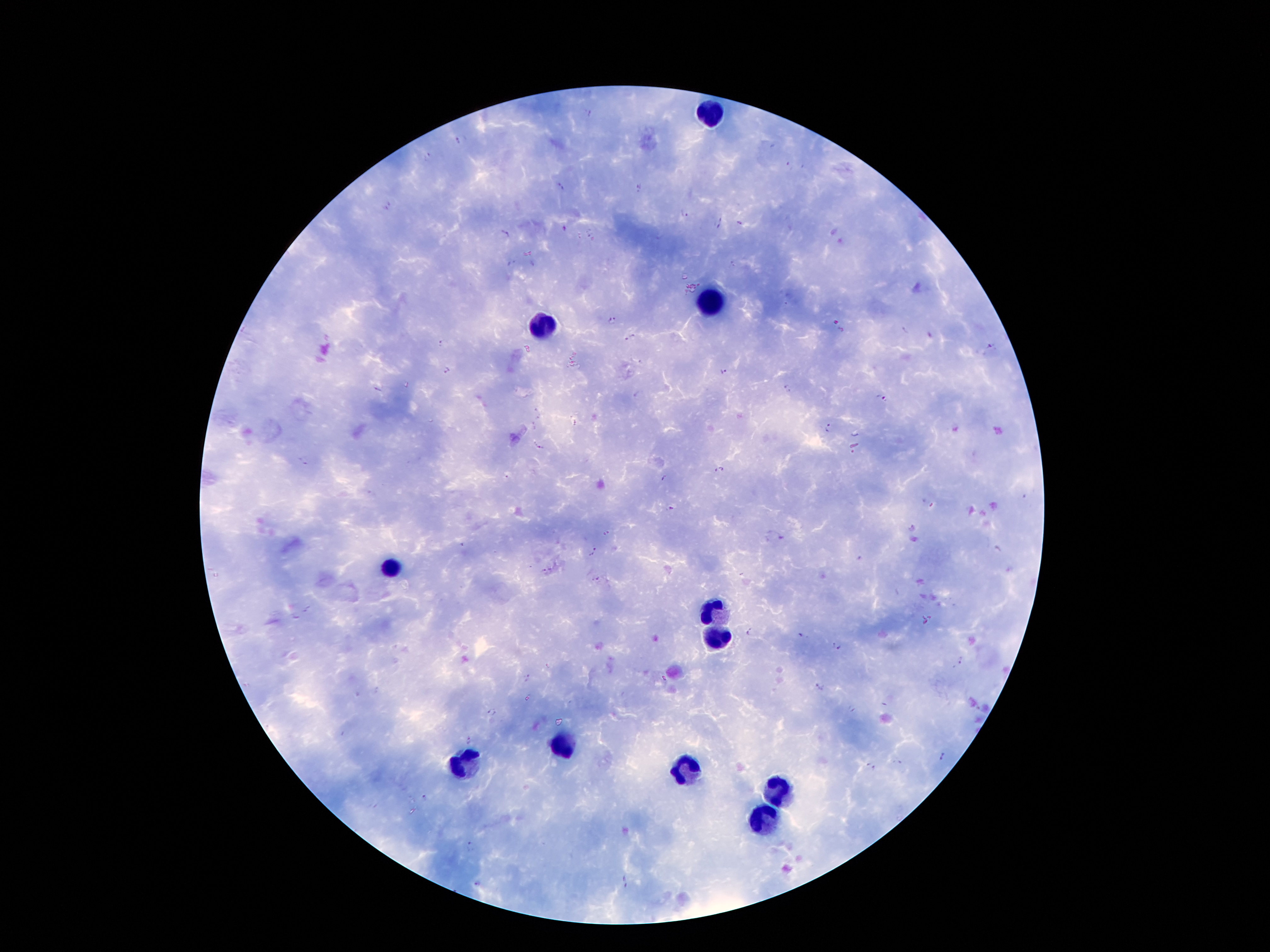
Approximate centers as (x, y) in pixels.
Summary:
  - Leukocyte locations: (711, 115), (711, 301), (543, 327), (391, 568), (707, 610), (716, 637), (561, 745), (464, 763), (680, 769), (773, 791), (764, 818)
  - Malaria parasite locations: (588, 112), (461, 140), (426, 157), (789, 166), (559, 187), (638, 188), (387, 206), (686, 215), (719, 216), (739, 223), (716, 227), (565, 228), (588, 231), (503, 235), (511, 263), (533, 263), (613, 321), (904, 330), (630, 338), (441, 343), (990, 345), (642, 361), (445, 369), (723, 371), (787, 389), (636, 395), (880, 399), (537, 411), (538, 418), (532, 423), (576, 423), (535, 428), (828, 428), (540, 447), (719, 469), (507, 477), (664, 478), (672, 507), (911, 529), (782, 539), (462, 545), (594, 551), (859, 559), (542, 570), (596, 579), (748, 631), (800, 636), (836, 646), (962, 660), (528, 677), (820, 686), (851, 708), (493, 714), (469, 741), (942, 756), (897, 762), (871, 766), (425, 797), (470, 846), (625, 881), (476, 885)
  - Image size: 1270×952 pixels
  - Preparation: thick blood film
  - Field of view: one from this slide
  - Capture: smartphone through the microscope eyepiece
  - Stain: Giemsa
  - Magnification: 100x
  - Patient malaria status: positive for Plasmodium falciparum